Assess the morphology of the red blood cells.
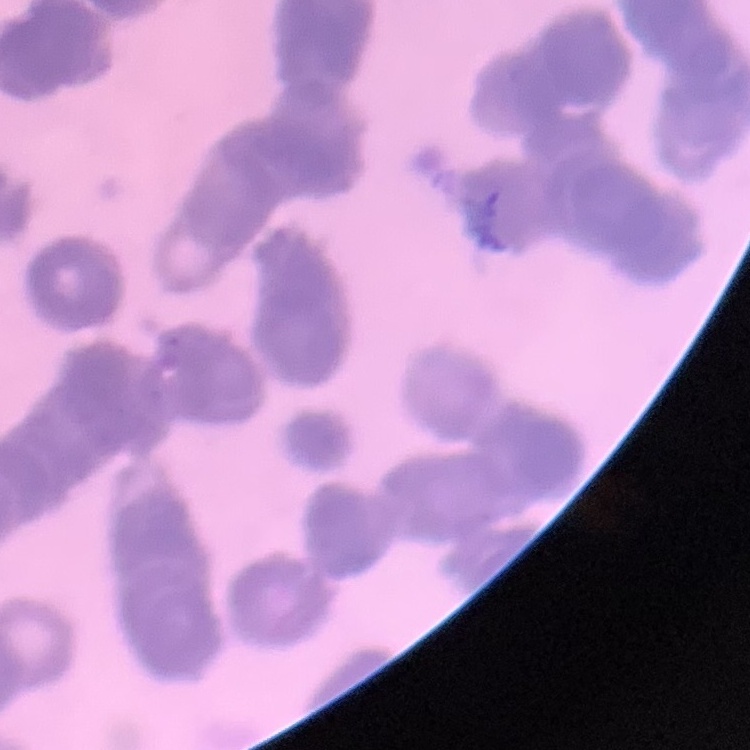
They show rouleaux formation.

One tile cut from a larger photomicrograph. Stained with either Field's or Giemsa. Thin blood smear.